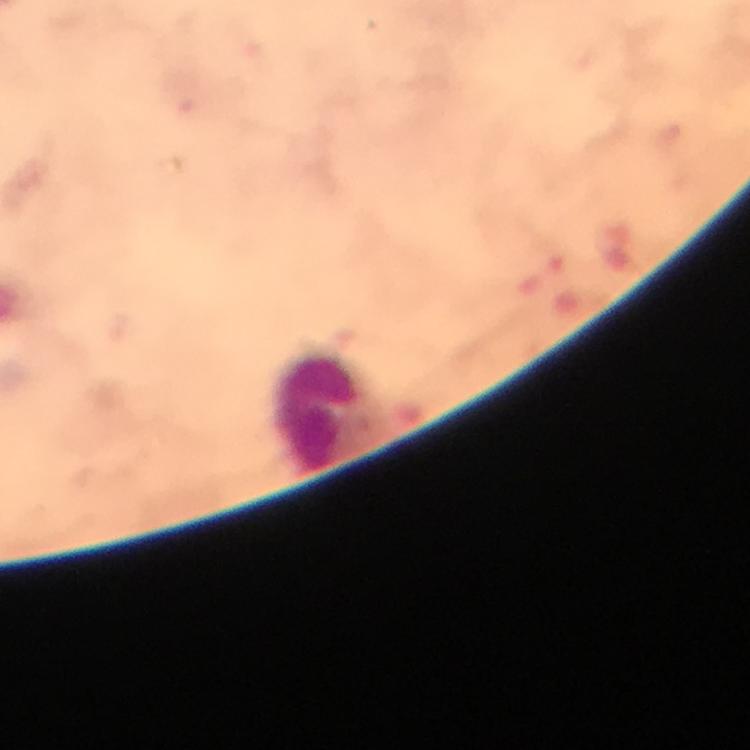

Approximate object centers, in pixels from the top-left corner.
Summary:
  - Leukocyte locations: (x=321, y=408)
  - Stain: Giemsa
  - Magnification: 100x
  - Capture: smartphone camera through the microscope
  - Image size: 750×750 pixels
  - Context: from a diagnostic examination for malaria
  - Immersion oil: applied
  - Plasmodium parasites: none seen
  - Cropped from: a single field of view
  - Preparation: thick blood film